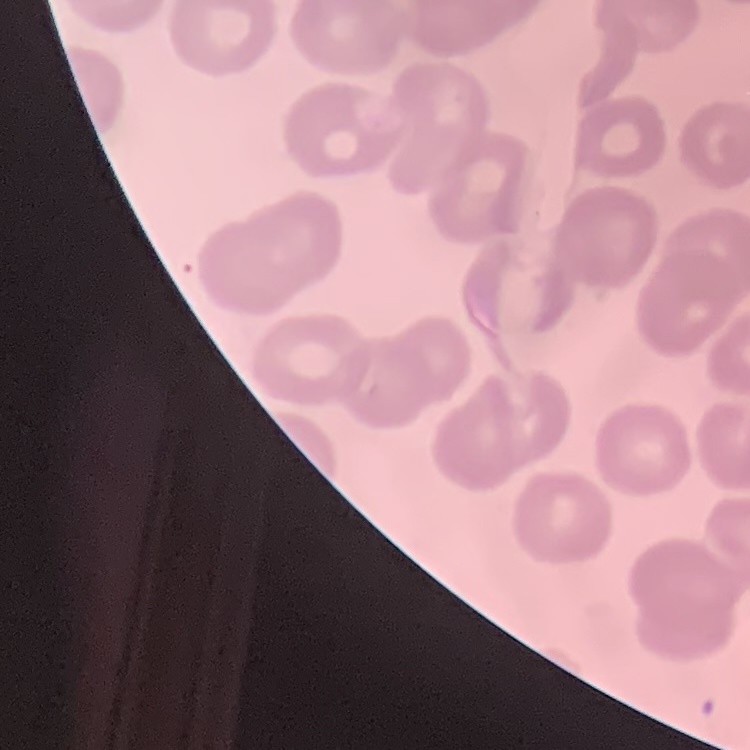
The erythrocytes exhibit no rouleaux formation. Square crop of a larger photomicrograph. Thin blood film. Field's or Giemsa stain.